Report the malaria status of this cell.
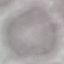
It is uninfected.

Thin blood smear. Automatically extracted cell patch, resized to 64 × 64 pixels. Photographed with a smartphone camera at the microscope eyepiece. Giemsa stain.